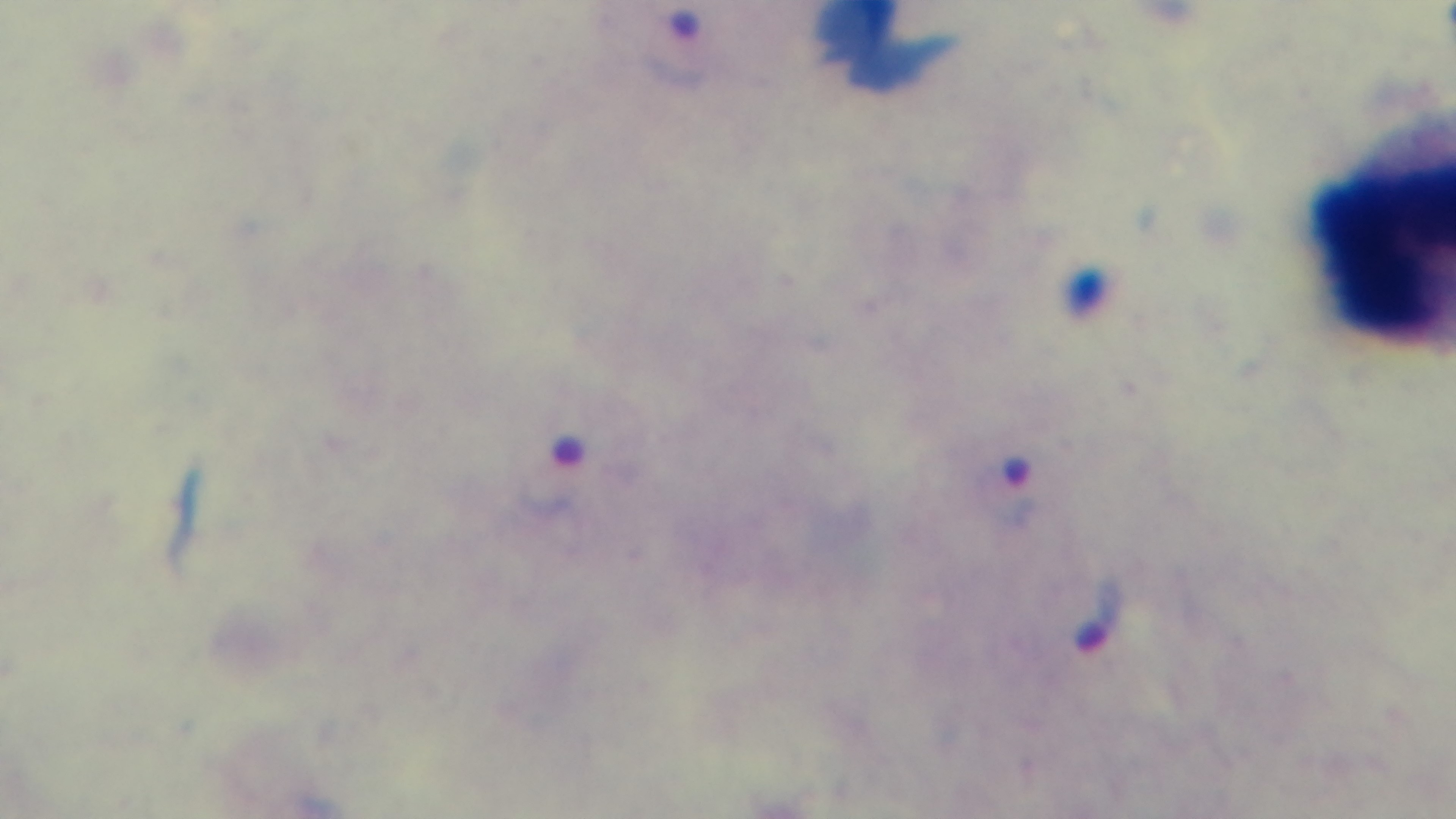
Summary:
  - Preparation: thick blood film
  - Malaria status: positive
  - Field of view: single
  - Capture: mounted 4K digital camera
  - Stain: Giemsa
  - Objective: 100x oil immersion
  - Modality: light microscopy